Locate every blood parasite and identify its species.
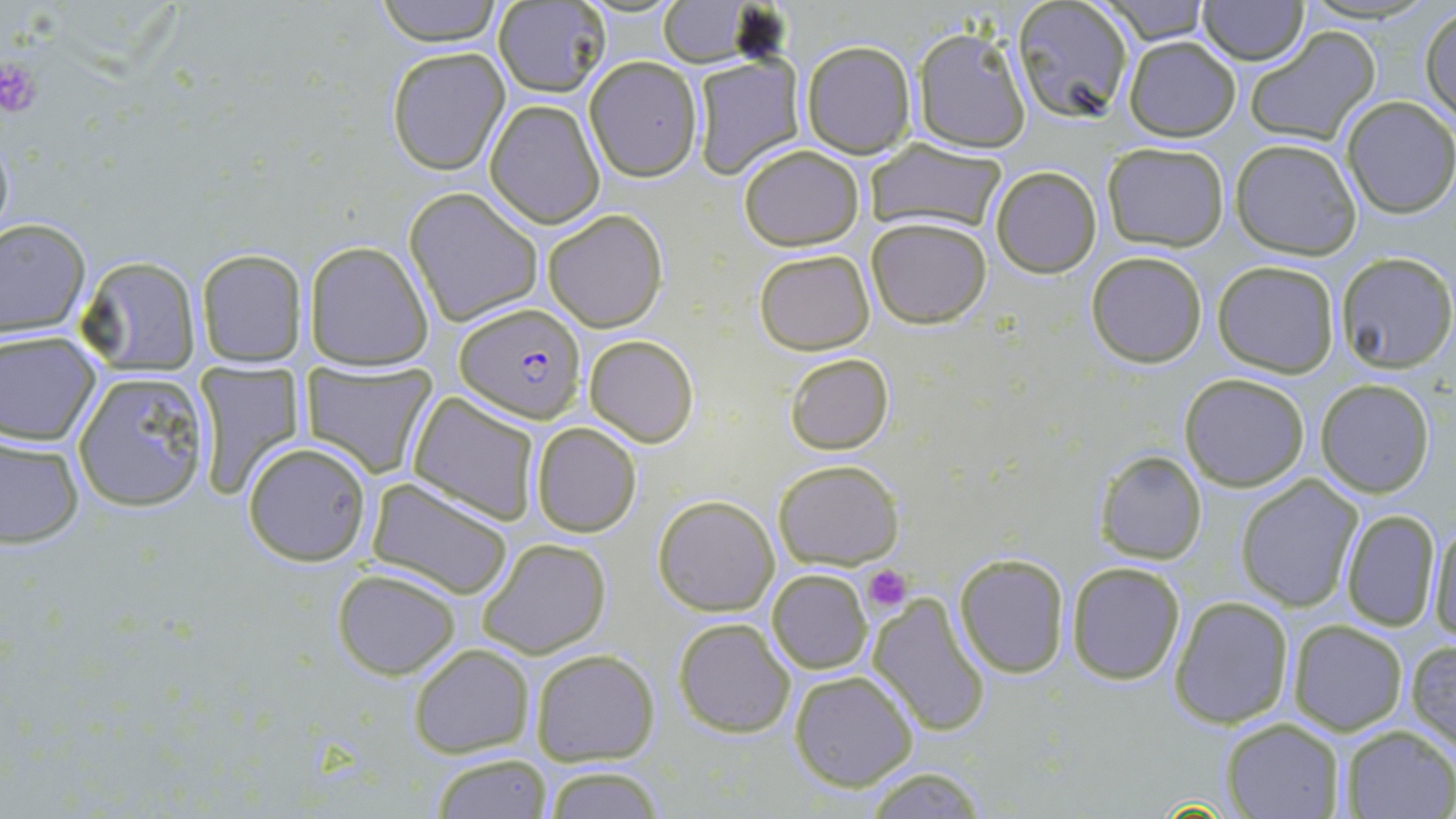
Approximate bounding boxes as [x1, y1, x2, y2] in pixels.
Plasmodium falciparum-infected red blood cells: [456, 304, 585, 422].
No Plasmodium ovale, Plasmodium malariae, Plasmodium vivax, Babesia divergens, or Trypanosoma brucei observed.

Summary:
  - Uninfected red blood cell locations: [374, 0, 506, 46], [1009, 0, 1136, 124], [1096, 0, 1213, 43], [1196, 0, 1308, 65], [491, 1, 611, 97], [658, 1, 756, 65], [1420, 7, 1456, 126], [1245, 26, 1381, 147], [913, 28, 1030, 153], [1123, 37, 1241, 141], [800, 39, 918, 159], [386, 46, 509, 176], [584, 56, 703, 182], [691, 56, 806, 179], [1342, 96, 1456, 218], [484, 98, 604, 228], [864, 138, 1009, 236], [1231, 138, 1363, 259], [1101, 141, 1231, 252], [738, 143, 866, 251], [989, 166, 1102, 278], [403, 187, 544, 326], [543, 208, 669, 332], [866, 217, 992, 329], [0, 218, 91, 340], [303, 241, 433, 372], [196, 248, 309, 367], [754, 249, 874, 354], [1086, 251, 1209, 368], [1333, 251, 1456, 372], [76, 256, 202, 378], [1213, 260, 1340, 377], [0, 331, 101, 446], [584, 334, 698, 448], [785, 352, 894, 456], [300, 360, 438, 477], [190, 361, 306, 501], [72, 371, 211, 513], [1179, 373, 1309, 491], [1315, 379, 1435, 497], [406, 393, 542, 526], [530, 420, 642, 538], [0, 436, 84, 549], [242, 441, 374, 566], [1098, 449, 1207, 564], [773, 459, 904, 569], [1237, 475, 1364, 612], [367, 478, 516, 600], [653, 494, 779, 616], [1341, 509, 1443, 633], [1427, 517, 1456, 642], [477, 538, 612, 659], [953, 552, 1071, 677], [1065, 562, 1185, 684], [331, 568, 461, 680], [768, 568, 872, 675], [867, 593, 991, 737], [1167, 594, 1294, 728], [672, 617, 795, 739], [1288, 621, 1408, 735], [1405, 636, 1456, 752], [408, 644, 535, 758], [531, 647, 661, 766], [790, 670, 919, 791], [1221, 718, 1345, 818], [1338, 725, 1456, 818], [429, 751, 553, 819], [538, 764, 669, 819], [861, 765, 993, 819]
  - Platelet locations: [0, 56, 43, 120], [864, 565, 910, 612]
  - Slide-level diagnosis: Plasmodium falciparum
  - Modality: optical microscopy
  - Stain: May-Grünwald-Giemsa
  - Magnification: 1000x
  - Field of view: one of a larger specimen
  - Image size: 1456×819 pixels
  - Preparation: thin blood smear